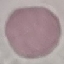
{
  "malaria_status": "uninfected",
  "capture": "smartphone through the microscope eyepiece",
  "preparation": "thin blood film",
  "stain": "Giemsa",
  "image_type": "cell patch, automatically extracted from a larger field of view and resized to 64 × 64 pixels"
}